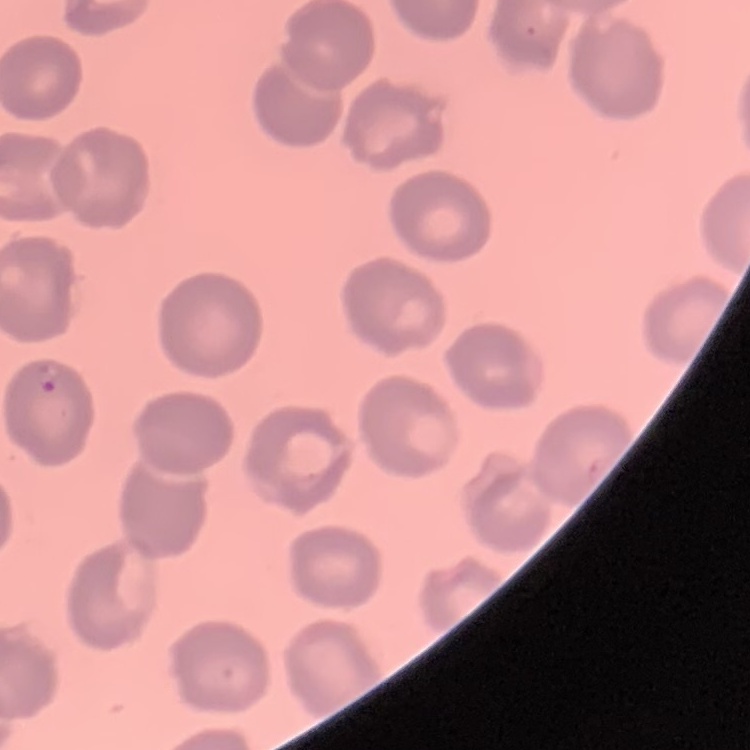 The erythrocytes exhibit no rouleaux formation. Field's or Giemsa stain. Square crop of a larger photomicrograph. Thin peripheral smear.